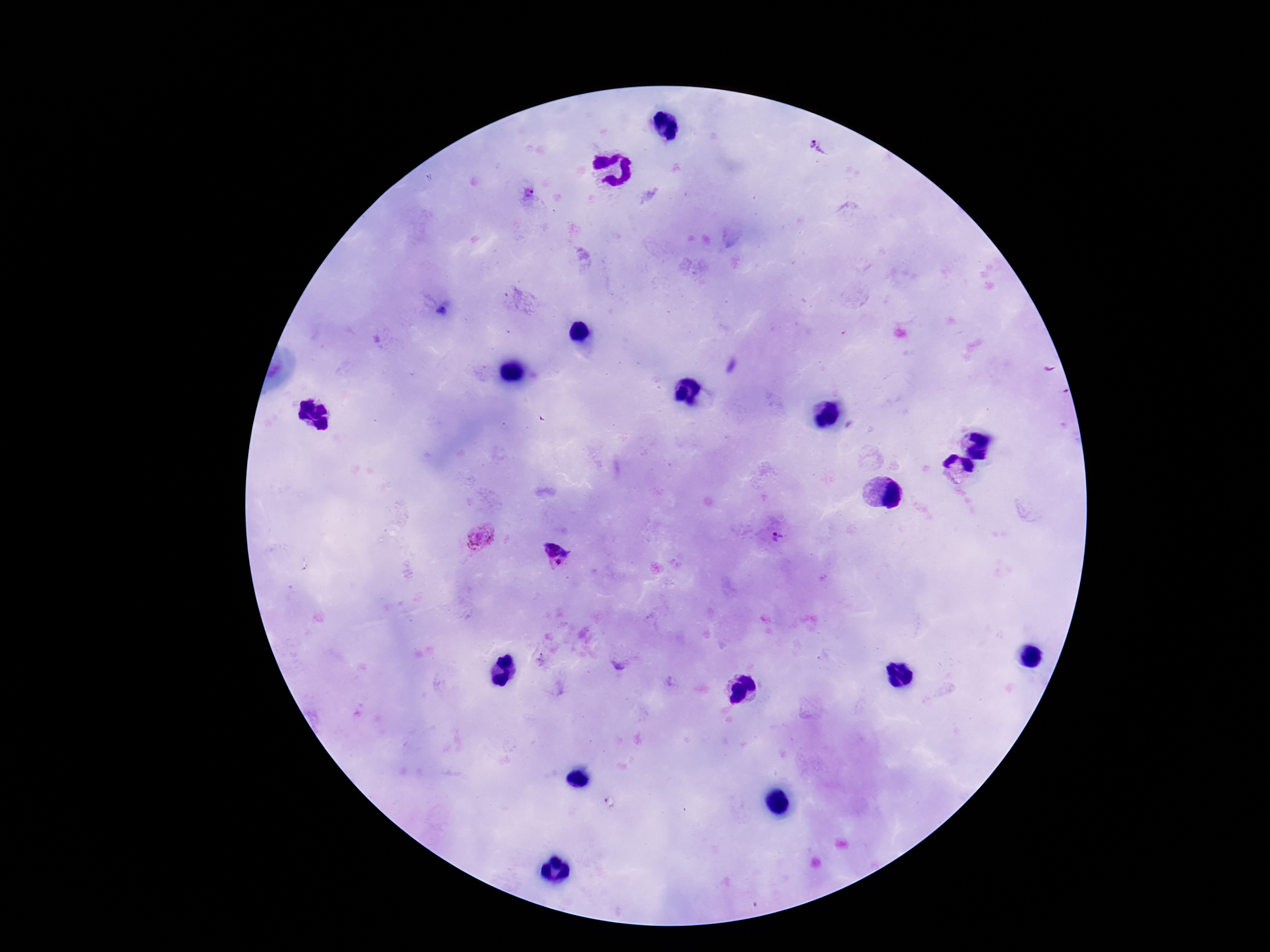
Approximate centers as [x, y] in pixels. Plasmodium parasite locations: [816, 149], [528, 190], [480, 537], [778, 540], [555, 554]. Patient malaria status: infected. One field from this slide. Photographed through the microscope eyepiece with a smartphone camera. Thick peripheral-blood smear. Image is 1270×952 pixels. Giemsa-stained preparation. 100x magnification.